Outline each blood parasite and name the species.
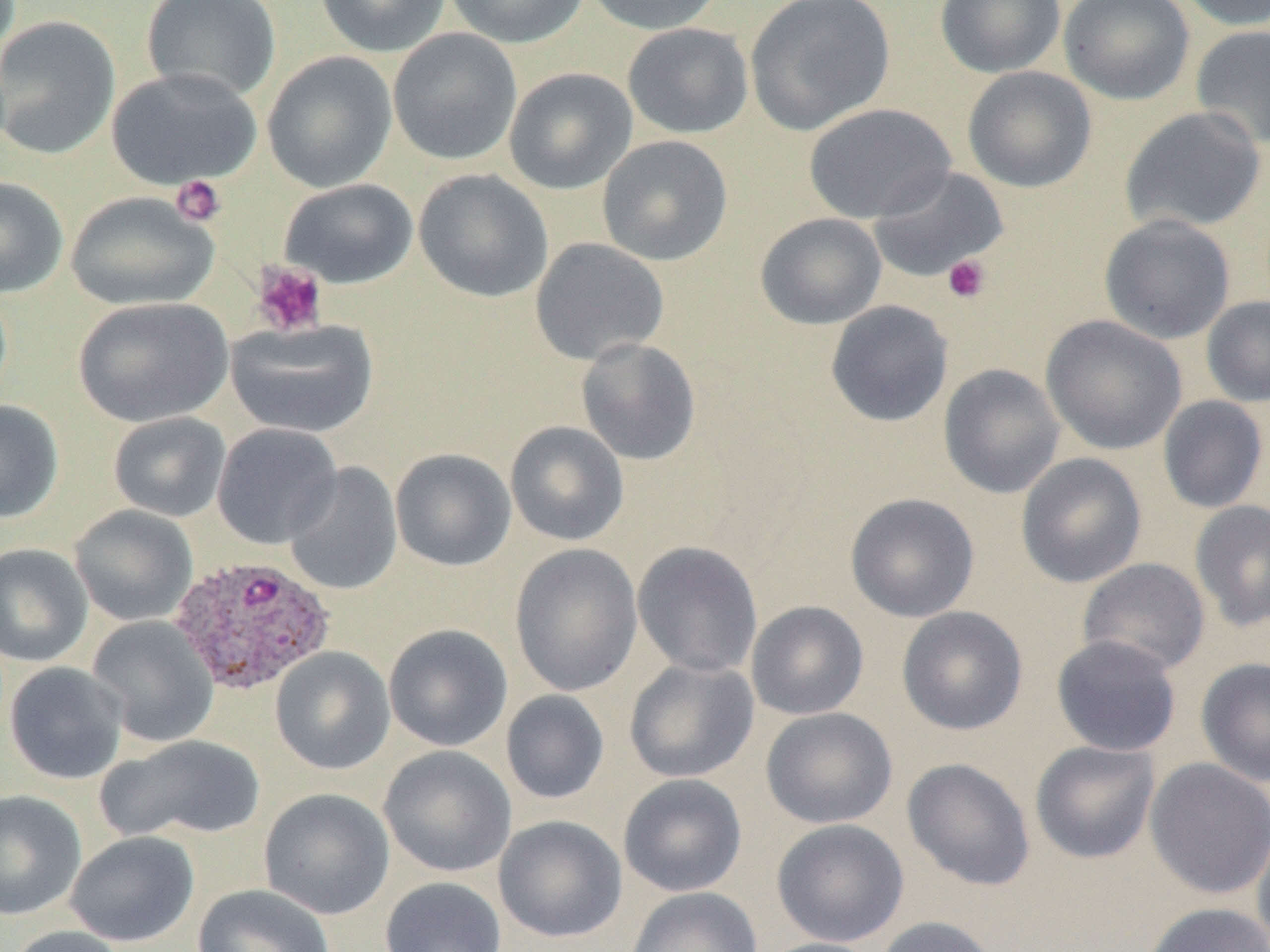

Approximate bounding boxes as (x1, y1, x2, y2) in pixels.
Plasmodium ovale-infected red blood cells: (169, 555, 336, 696).
No Plasmodium falciparum, Plasmodium malariae, Plasmodium vivax, Babesia divergens, or Trypanosoma brucei observed.

Uninfected red blood cell locations: (142, 0, 281, 103), (314, 0, 452, 58), (444, 0, 590, 49), (582, 0, 726, 35), (744, 0, 895, 136), (935, 0, 1067, 78), (1059, 0, 1195, 106), (1176, 0, 1270, 31), (0, 15, 121, 160), (622, 22, 754, 139), (1190, 24, 1270, 150), (388, 28, 523, 166), (262, 50, 397, 193), (962, 66, 1097, 193), (105, 67, 263, 190), (504, 67, 637, 194), (804, 103, 956, 223), (1119, 106, 1267, 235), (597, 134, 733, 266), (868, 166, 1009, 282), (413, 168, 553, 302), (0, 176, 69, 298), (279, 178, 418, 289), (65, 190, 219, 311), (755, 212, 887, 329), (1099, 213, 1236, 344), (529, 238, 669, 365), (1201, 295, 1270, 408), (73, 296, 233, 428), (825, 300, 954, 427), (1041, 315, 1188, 455), (225, 319, 379, 439), (576, 337, 702, 465), (938, 363, 1065, 499), (1158, 395, 1269, 514), (0, 399, 64, 523), (108, 411, 231, 522), (505, 421, 629, 546), (211, 423, 343, 549), (391, 448, 516, 571), (1016, 452, 1147, 588), (283, 461, 403, 596), (845, 492, 980, 623), (1189, 499, 1270, 632), (69, 505, 198, 626), (632, 540, 763, 678), (0, 543, 93, 667), (510, 543, 644, 697), (1077, 558, 1211, 676), (746, 601, 869, 720), (896, 606, 1028, 735), (87, 615, 220, 748), (383, 623, 513, 751), (1051, 635, 1182, 757), (270, 646, 395, 775), (1195, 656, 1270, 787), (624, 659, 759, 783), (4, 662, 129, 785), (500, 689, 610, 805), (761, 707, 898, 829), (97, 734, 266, 845), (1030, 740, 1161, 864), (378, 745, 517, 878), (902, 757, 1035, 891), (1144, 757, 1270, 900), (618, 773, 747, 897), (258, 787, 395, 919), (0, 789, 87, 921), (493, 815, 627, 943), (771, 818, 910, 947), (1251, 820, 1270, 952), (65, 831, 199, 947), (379, 876, 507, 952), (193, 883, 336, 952), (626, 887, 763, 952), (1141, 901, 1270, 952), (873, 915, 1002, 952), (5, 925, 130, 952), (757, 937, 886, 952). Platelet locations: (170, 175, 226, 227), (943, 254, 992, 304), (251, 261, 328, 337). Slide-level diagnosis: Plasmodium ovale. One field of a larger specimen. Light microscopy. Thin blood smear. 1000x magnification. Image is 1270×952 pixels.